Outline every artifact (platelet-like body, stain precipitate, or debris).
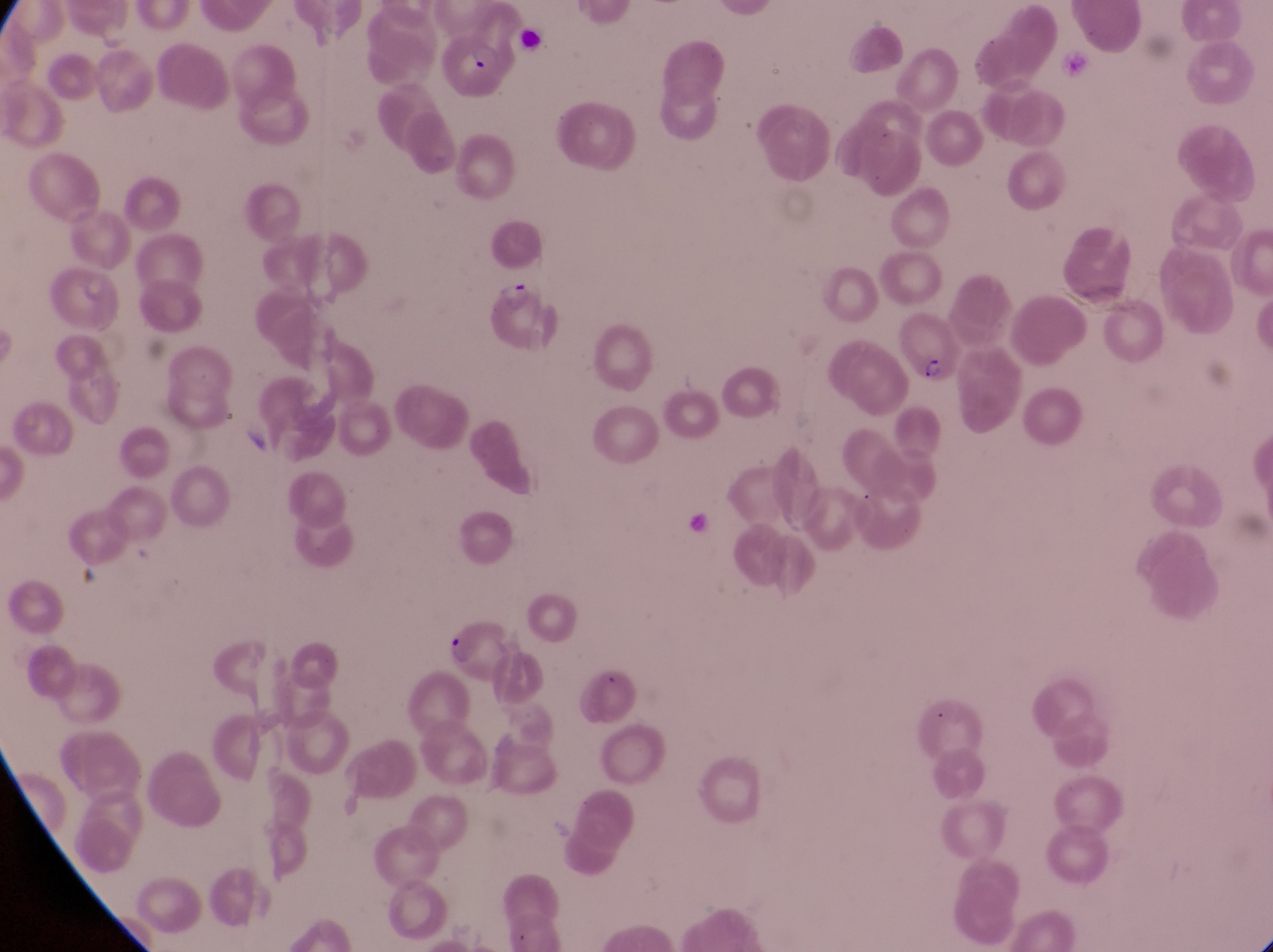
Approximate bounding boxes as left top right bottom in pixels.
Artifacts (platelet-like body, stain precipitate, or debris): 239 412 274 452; 686 504 714 539.

Summary:
  - Trophozoite locations: 495 270 528 313
  - Parasitised red blood cell locations: 441 37 502 106; 893 307 955 387; 442 619 517 677
  - Capture: smartphone photograph through the eyepiece of an Olympus CX-23 microscope
  - Image size: 1273×952 pixels
  - Magnification: 1000x
  - Preparation: thin blood film
  - Country: Uganda
  - Field of view: single